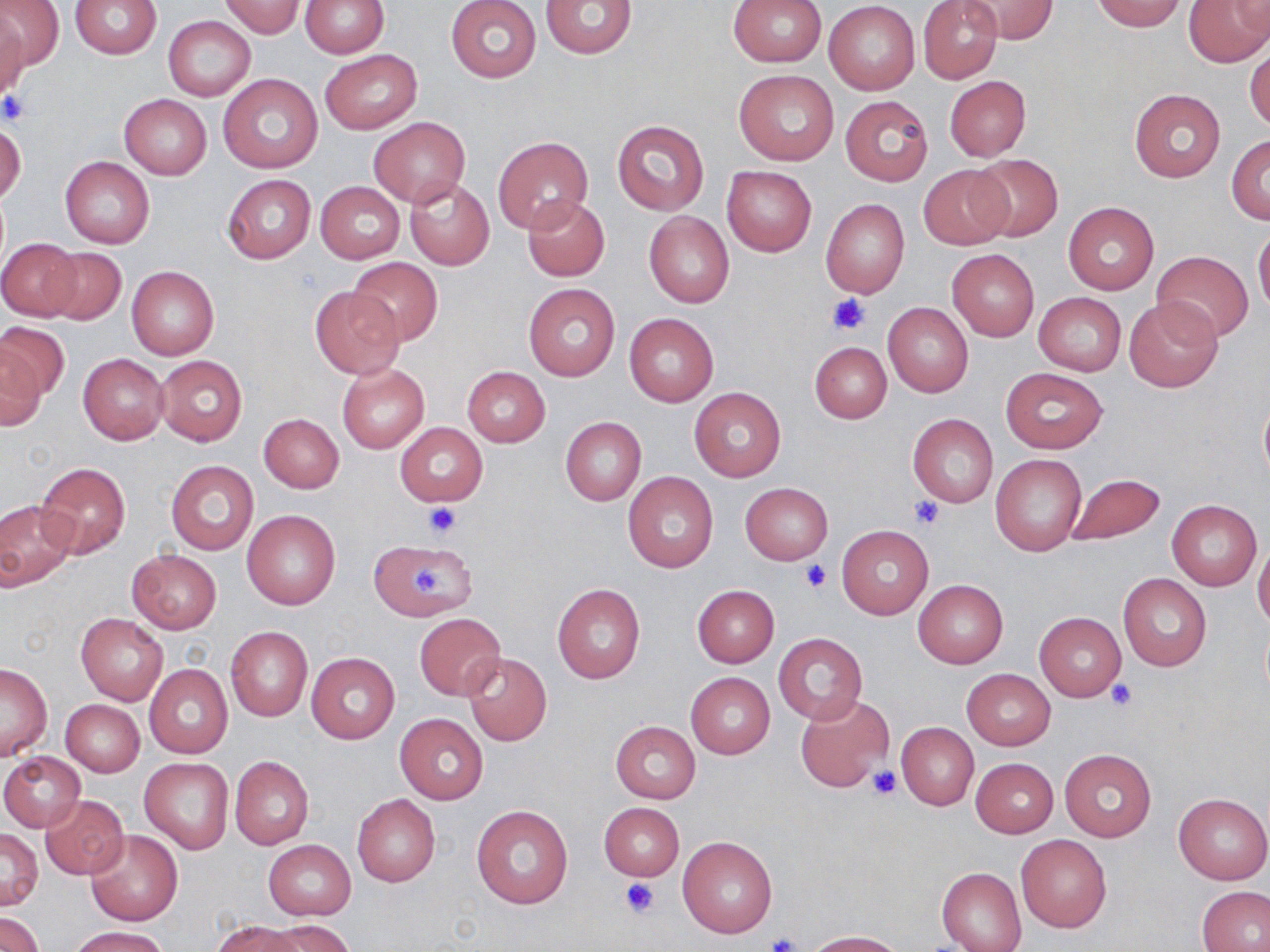
Summary:
  - Coordinate format: approximate bounding boxes as named x1/y1/x2/y2 corners in pixels
  - Uninfected red blood cell locations: (x1=0, y1=0, x2=64, y2=73), (x1=71, y1=0, x2=162, y2=59), (x1=542, y1=0, x2=638, y2=58), (x1=728, y1=0, x2=827, y2=67), (x1=918, y1=0, x2=1003, y2=84), (x1=961, y1=0, x2=1057, y2=43), (x1=1093, y1=0, x2=1187, y2=32), (x1=1184, y1=0, x2=1268, y2=67), (x1=219, y1=1, x2=305, y2=37), (x1=300, y1=1, x2=388, y2=57), (x1=446, y1=1, x2=541, y2=82), (x1=824, y1=1, x2=920, y2=94), (x1=1228, y1=2, x2=1270, y2=35), (x1=0, y1=8, x2=28, y2=99), (x1=164, y1=15, x2=255, y2=102), (x1=1245, y1=47, x2=1270, y2=133), (x1=321, y1=49, x2=422, y2=134), (x1=735, y1=69, x2=839, y2=166), (x1=219, y1=73, x2=322, y2=173), (x1=944, y1=75, x2=1030, y2=161), (x1=1129, y1=88, x2=1226, y2=183), (x1=119, y1=93, x2=212, y2=180), (x1=841, y1=95, x2=932, y2=186), (x1=368, y1=116, x2=471, y2=208), (x1=612, y1=118, x2=710, y2=216), (x1=0, y1=122, x2=26, y2=205), (x1=493, y1=136, x2=592, y2=234), (x1=1227, y1=136, x2=1270, y2=223), (x1=967, y1=153, x2=1063, y2=241), (x1=59, y1=155, x2=154, y2=249), (x1=918, y1=165, x2=1014, y2=250), (x1=722, y1=166, x2=817, y2=256), (x1=221, y1=174, x2=317, y2=263), (x1=405, y1=177, x2=494, y2=270), (x1=315, y1=182, x2=405, y2=262), (x1=523, y1=197, x2=610, y2=282), (x1=820, y1=199, x2=909, y2=299), (x1=1062, y1=202, x2=1158, y2=294), (x1=644, y1=212, x2=733, y2=308), (x1=1253, y1=229, x2=1270, y2=314), (x1=0, y1=239, x2=82, y2=320), (x1=42, y1=246, x2=126, y2=324), (x1=946, y1=247, x2=1040, y2=342), (x1=1151, y1=251, x2=1254, y2=343), (x1=348, y1=256, x2=442, y2=344), (x1=126, y1=266, x2=219, y2=359), (x1=524, y1=283, x2=619, y2=381), (x1=310, y1=286, x2=405, y2=379), (x1=1034, y1=292, x2=1126, y2=376), (x1=1123, y1=297, x2=1223, y2=393), (x1=882, y1=304, x2=973, y2=398), (x1=624, y1=312, x2=719, y2=407), (x1=0, y1=320, x2=68, y2=406), (x1=1, y1=339, x2=47, y2=431), (x1=810, y1=342, x2=892, y2=423), (x1=78, y1=354, x2=168, y2=444), (x1=156, y1=355, x2=247, y2=445), (x1=338, y1=364, x2=429, y2=452), (x1=461, y1=367, x2=550, y2=447), (x1=999, y1=367, x2=1108, y2=453), (x1=688, y1=386, x2=786, y2=482), (x1=1258, y1=392, x2=1270, y2=484), (x1=258, y1=413, x2=344, y2=492), (x1=908, y1=414, x2=998, y2=508), (x1=560, y1=417, x2=646, y2=506), (x1=395, y1=423, x2=487, y2=506), (x1=991, y1=454, x2=1087, y2=557), (x1=166, y1=461, x2=258, y2=555), (x1=35, y1=463, x2=130, y2=558), (x1=1064, y1=471, x2=1166, y2=546), (x1=623, y1=473, x2=718, y2=572), (x1=740, y1=483, x2=833, y2=564), (x1=0, y1=497, x2=78, y2=591), (x1=1166, y1=498, x2=1262, y2=591), (x1=241, y1=509, x2=340, y2=610), (x1=836, y1=525, x2=933, y2=620), (x1=369, y1=539, x2=477, y2=620), (x1=1253, y1=541, x2=1270, y2=631), (x1=126, y1=549, x2=222, y2=633), (x1=1118, y1=574, x2=1211, y2=671), (x1=913, y1=580, x2=1008, y2=667), (x1=552, y1=584, x2=646, y2=684), (x1=691, y1=585, x2=778, y2=667), (x1=1035, y1=612, x2=1126, y2=701), (x1=76, y1=613, x2=168, y2=704), (x1=414, y1=613, x2=506, y2=700), (x1=225, y1=625, x2=313, y2=722), (x1=773, y1=632, x2=868, y2=726), (x1=306, y1=652, x2=399, y2=743), (x1=463, y1=653, x2=552, y2=745), (x1=0, y1=662, x2=52, y2=760), (x1=144, y1=663, x2=233, y2=758), (x1=962, y1=669, x2=1055, y2=749), (x1=686, y1=672, x2=774, y2=758), (x1=795, y1=694, x2=894, y2=793), (x1=60, y1=699, x2=144, y2=776), (x1=394, y1=713, x2=489, y2=804), (x1=610, y1=721, x2=699, y2=804), (x1=896, y1=721, x2=978, y2=811), (x1=1059, y1=749, x2=1156, y2=843), (x1=0, y1=752, x2=86, y2=832), (x1=230, y1=756, x2=314, y2=850), (x1=139, y1=758, x2=233, y2=854), (x1=972, y1=758, x2=1058, y2=837), (x1=1174, y1=793, x2=1270, y2=884), (x1=352, y1=794, x2=440, y2=886), (x1=40, y1=795, x2=129, y2=880), (x1=599, y1=803, x2=684, y2=881), (x1=471, y1=804, x2=573, y2=908), (x1=84, y1=829, x2=182, y2=925), (x1=0, y1=830, x2=43, y2=909), (x1=1016, y1=834, x2=1112, y2=932), (x1=677, y1=836, x2=777, y2=938), (x1=262, y1=839, x2=357, y2=920), (x1=937, y1=867, x2=1025, y2=951), (x1=1197, y1=886, x2=1270, y2=952), (x1=0, y1=910, x2=44, y2=952), (x1=271, y1=919, x2=357, y2=952), (x1=213, y1=920, x2=300, y2=952), (x1=70, y1=926, x2=171, y2=952), (x1=804, y1=931, x2=903, y2=951)
  - Platelet locations: (x1=0, y1=91, x2=33, y2=124), (x1=828, y1=293, x2=871, y2=334), (x1=908, y1=495, x2=945, y2=530), (x1=422, y1=502, x2=461, y2=539), (x1=800, y1=560, x2=833, y2=592), (x1=409, y1=569, x2=447, y2=596), (x1=1108, y1=680, x2=1136, y2=711), (x1=867, y1=765, x2=902, y2=801), (x1=620, y1=879, x2=662, y2=918), (x1=763, y1=933, x2=802, y2=952)
  - Slide-level diagnosis: no evidence of blood parasites
  - Field of view: single
  - Stain: May-Grünwald-Giemsa
  - Modality: light microscopy
  - Preparation: thin blood smear
  - Image size: 1270×952 pixels
  - Magnification: 1000x